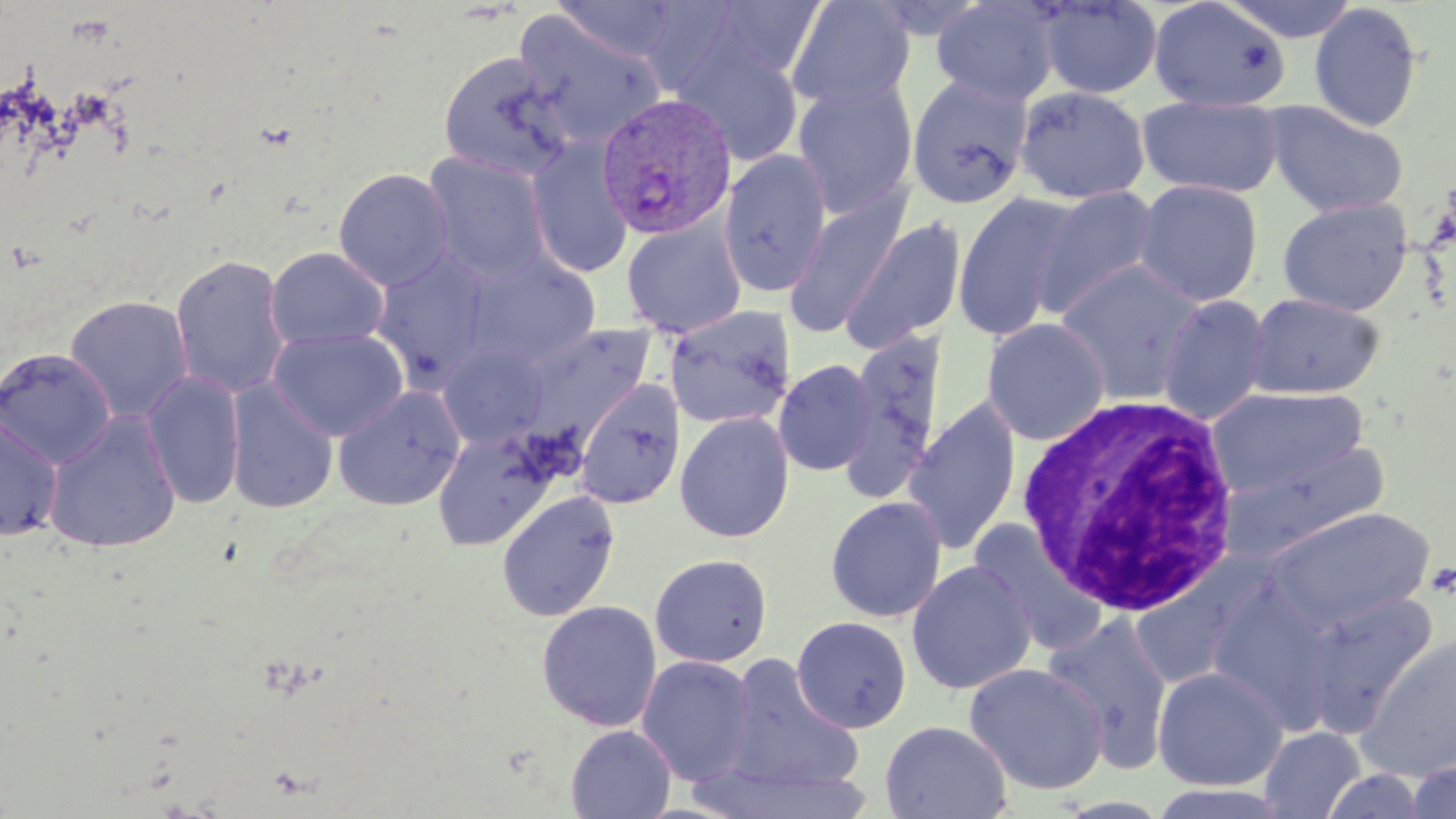

{
  "slide_level_diagnosis": "Plasmodium vivax",
  "uninfected_red_blood_cell_locations": "approximate bounding boxes as (x1,y1)-(x2,y2) corner pairs in pixels: (550,0)-(685,63), (704,0)-(829,81), (1036,0)-(1163,100), (1148,0)-(1292,113), (1219,0)-(1362,43), (785,1)-(914,112), (929,1)-(1060,107), (1309,2)-(1424,132), (514,10)-(667,148), (673,37)-(804,167), (438,51)-(574,181), (905,76)-(1034,209), (791,81)-(918,218), (1013,85)-(1150,205), (1136,96)-(1284,199), (1262,101)-(1409,217), (526,140)-(634,279), (718,150)-(832,298), (423,152)-(551,284), (333,168)-(453,289), (1132,179)-(1264,306), (1032,186)-(1161,318), (783,188)-(913,340), (951,191)-(1078,342), (1277,197)-(1413,316), (838,214)-(967,353), (622,219)-(746,338), (265,246)-(390,350), (371,251)-(493,386), (170,253)-(292,399), (463,253)-(601,368), (1055,260)-(1208,404), (1245,292)-(1385,399), (64,294)-(194,423), (1157,294)-(1270,425), (664,304)-(795,430), (981,318)-(1110,445), (516,324)-(656,452), (268,327)-(409,441), (841,329)-(948,502), (438,342)-(550,449), (0,347)-(117,468), (773,358)-(877,477), (140,371)-(246,510), (225,379)-(339,514), (574,379)-(685,509), (1208,384)-(1369,502), (333,385)-(466,510), (902,399)-(1022,556), (43,411)-(182,553), (674,411)-(794,544), (0,415)-(64,541), (431,428)-(556,550), (1221,438)-(1390,560), (495,490)-(620,622), (825,496)-(947,623), (1263,507)-(1433,632), (970,520)-(1109,655), (649,553)-(773,668), (907,559)-(1037,695), (1300,589)-(1440,736), (536,599)-(662,732), (1041,613)-(1175,769), (791,616)-(912,733), (1356,632)-(1456,780), (637,655)-(756,786), (720,656)-(864,795), (964,662)-(1109,795), (1152,665)-(1288,791), (879,720)-(1012,819), (565,724)-(677,819), (1260,727)-(1365,818), (1401,756)-(1456,819), (687,761)-(876,818)",
  "white_blood_cell_locations": "approximate bounding boxes as (x1,y1)-(x2,y2) corner pairs in pixels: (1017,394)-(1245,618)",
  "field_of_view": "one of a larger specimen",
  "magnification": "1000x",
  "preparation": "thin blood film",
  "stain": "May-Grünwald-Giemsa",
  "plasmodium_vivax_infected_red_blood_cell_locations": "approximate bounding boxes as (x1,y1)-(x2,y2) corner pairs in pixels: (595,93)-(738,240)",
  "modality": "light microscopy",
  "image_size": "1456×819 pixels"
}